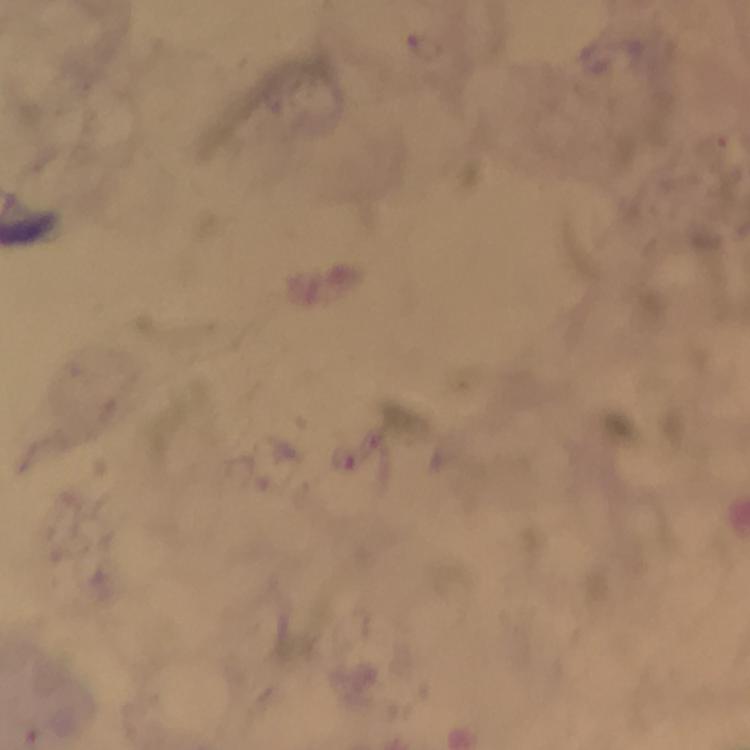
context: from a malaria diagnostic workup
capture: smartphone mounted on the microscope
image_size: 750×750 pixels
immersion_oil: used
cropped_from: a single field of view
preparation: thick blood film
magnification: 100x
stain: Giemsa
malaria_parasite_locations: 'approximate object centers, in pixels from the top-left corner: (x=342, y=460)'